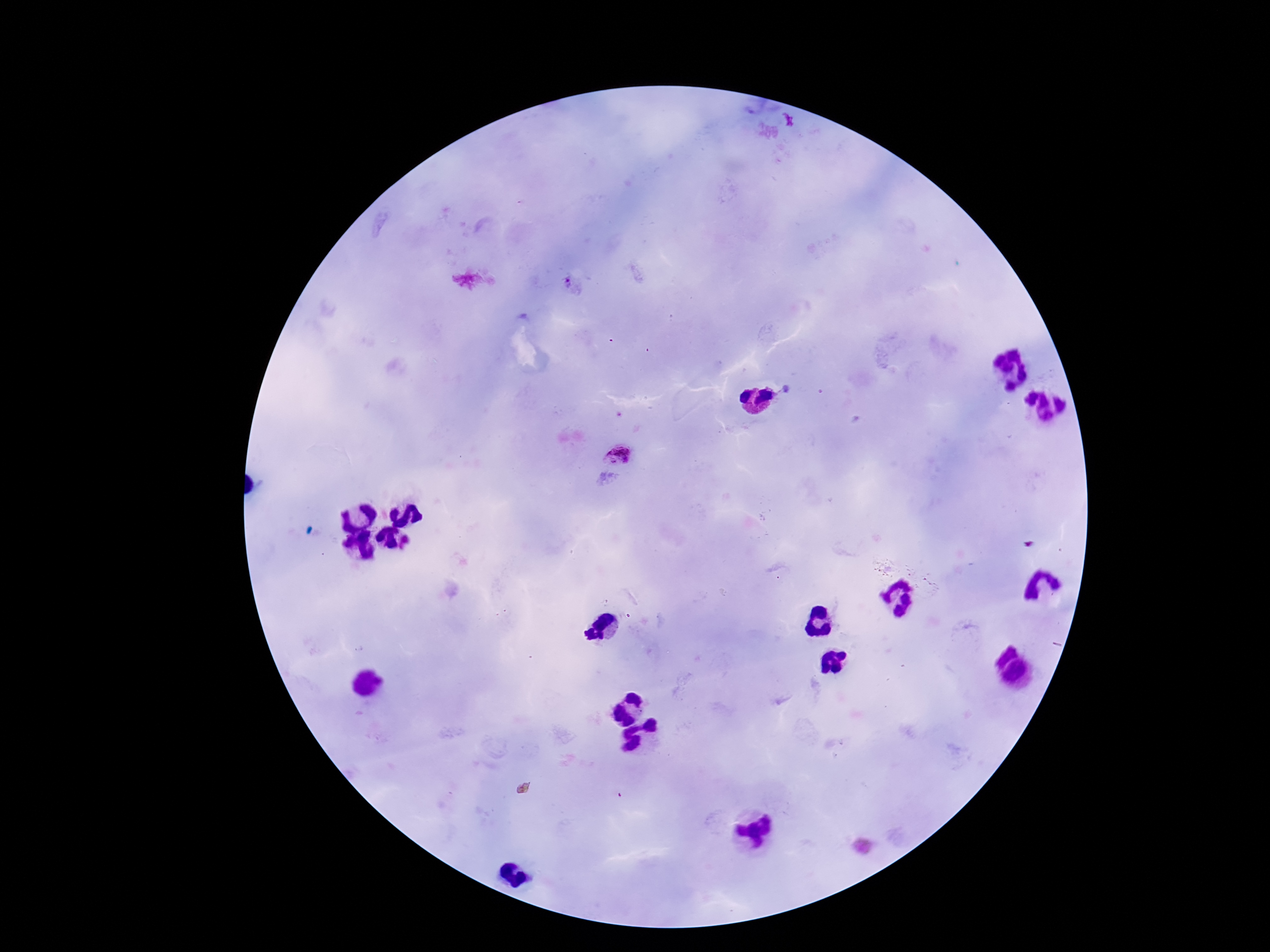
preparation = thick peripheral-blood smear
capture = smartphone camera through the microscope eyepiece
stain = Giemsa
magnification = 100x
Plasmodium parasite locations = approximate centers as (x, y) in pixels: (570, 286), (619, 453), (408, 541)
field of view = one from this slide
patient malaria status = infected
image size = 1270×952 pixels